State the blood parasite species.
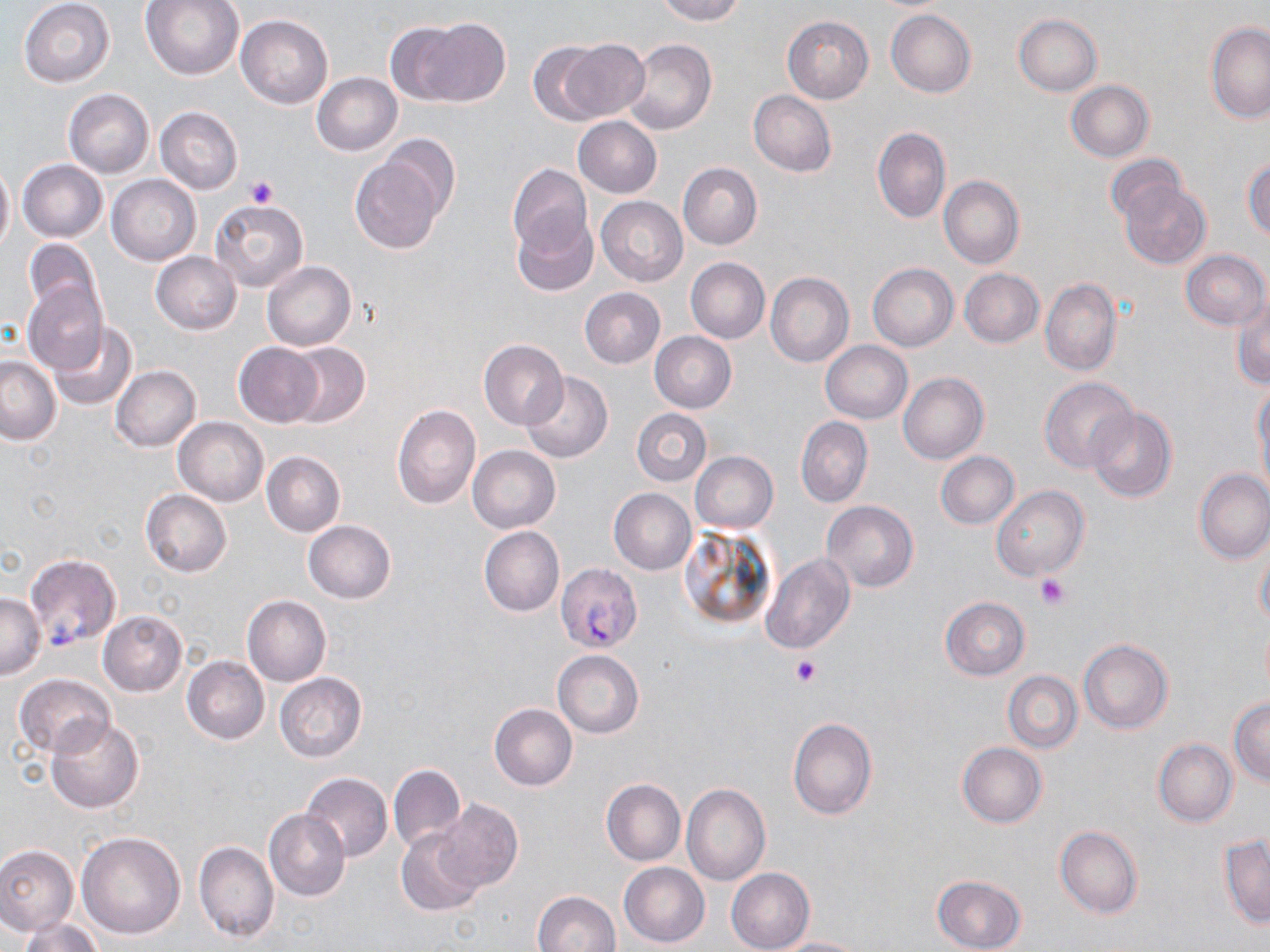

Plasmodium falciparum.

field_of_view: single
stain: May-Grünwald-Giemsa
preparation: thin blood smear
magnification: 1000x
platelet_locations: 'approximate bounding boxes as (x1, y1, x2, y2) in pixels: (246, 175, 278, 209), (1034, 572, 1070, 610), (790, 654, 822, 686)'
modality: light microscopy
image_size: 1270×952 pixels
uninfected_red_blood_cell_locations: 'approximate bounding boxes as (x1, y1, x2, y2) in pixels: (141, 0, 245, 81), (657, 0, 745, 25), (20, 1, 115, 87), (886, 9, 977, 97), (1014, 13, 1102, 96), (235, 14, 332, 108), (783, 16, 874, 103), (400, 17, 510, 107), (1207, 22, 1270, 124), (554, 39, 649, 124), (625, 40, 717, 135), (527, 43, 610, 125), (312, 73, 402, 155), (1065, 81, 1153, 162), (63, 89, 154, 177), (748, 90, 836, 177), (156, 107, 242, 193), (574, 116, 662, 197), (873, 127, 951, 225), (377, 134, 461, 222), (349, 150, 449, 254), (1105, 155, 1187, 228), (1243, 156, 1270, 240), (17, 160, 107, 242), (0, 162, 14, 253), (678, 162, 763, 250), (507, 163, 593, 255), (106, 174, 201, 265), (939, 175, 1024, 269), (1118, 177, 1211, 270), (596, 197, 687, 287), (210, 199, 308, 293), (512, 211, 598, 295), (21, 238, 103, 321), (1181, 249, 1269, 330), (150, 251, 241, 334), (685, 258, 769, 343), (262, 261, 356, 351), (867, 263, 958, 350), (959, 269, 1045, 349), (765, 272, 854, 368), (1041, 278, 1122, 378), (22, 280, 108, 375), (580, 288, 665, 368), (1231, 296, 1270, 388), (49, 323, 137, 410), (650, 332, 737, 412), (478, 339, 569, 430), (820, 341, 912, 423), (234, 342, 323, 426), (281, 342, 371, 429), (0, 356, 61, 444), (111, 366, 200, 452), (520, 372, 613, 463), (898, 373, 988, 464), (1039, 377, 1137, 472), (1253, 382, 1270, 489), (391, 404, 481, 509), (1085, 405, 1178, 504), (632, 409, 711, 486), (174, 417, 268, 506), (796, 417, 873, 508), (468, 445, 560, 532), (261, 451, 345, 536), (690, 451, 778, 532), (936, 451, 1019, 529), (1194, 469, 1270, 563), (991, 485, 1088, 581), (608, 488, 697, 574), (140, 490, 232, 578), (821, 499, 918, 592), (303, 521, 396, 604), (478, 526, 564, 617), (1256, 545, 1270, 629), (761, 553, 855, 654), (0, 592, 46, 679), (242, 595, 331, 685), (940, 597, 1031, 680), (98, 611, 187, 696), (1078, 640, 1174, 734), (552, 650, 645, 738), (182, 656, 268, 745), (1003, 672, 1082, 753), (14, 673, 115, 760), (274, 673, 366, 762), (1229, 697, 1270, 785), (489, 703, 577, 791), (46, 716, 143, 813), (787, 716, 878, 820), (1153, 740, 1237, 826), (956, 742, 1048, 828), (389, 764, 465, 853), (300, 772, 392, 862), (601, 779, 685, 866), (681, 783, 770, 887), (434, 799, 523, 893), (263, 809, 350, 900), (1055, 825, 1143, 919), (397, 829, 484, 918), (77, 831, 186, 938), (1219, 835, 1269, 928), (194, 840, 278, 942), (0, 846, 77, 936), (619, 862, 709, 947), (726, 867, 815, 952), (931, 875, 1027, 952), (533, 891, 620, 952), (20, 917, 104, 952), (771, 937, 868, 952)'
plasmodium_falciparum_infected_red_blood_cell_locations: 'approximate bounding boxes as (x1, y1, x2, y2) in pixels: (23, 554, 122, 650), (556, 563, 642, 652)'